Assess the morphology of the erythrocytes.
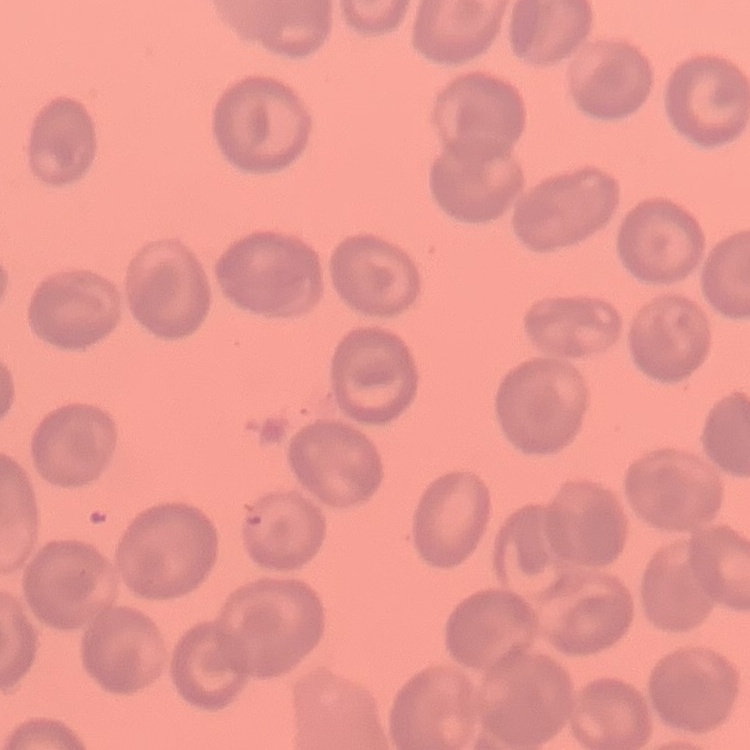
No rouleaux formation.

stain = Field's or Giemsa
preparation = thin blood smear
image type = square crop of a larger photomicrograph